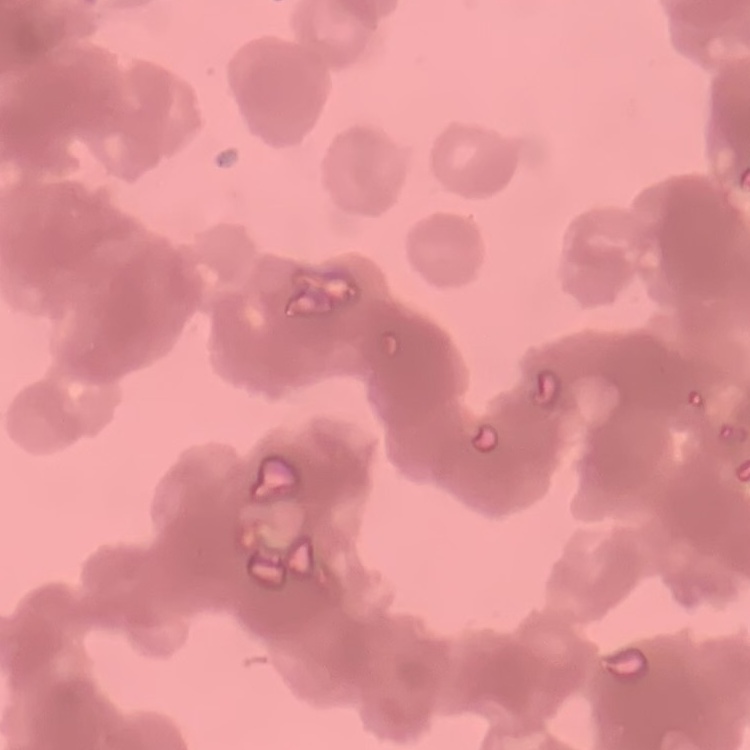

Summary:
  - Erythrocyte morphology: rouleaux formation
  - Stain: Field's or Giemsa
  - Image type: square crop of a larger photomicrograph
  - Preparation: thin blood film